Report the malaria status of this cell.
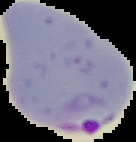
Parasitized.

From a thin blood smear. Image is 136×142 pixels. Segmented cell region on a black background.